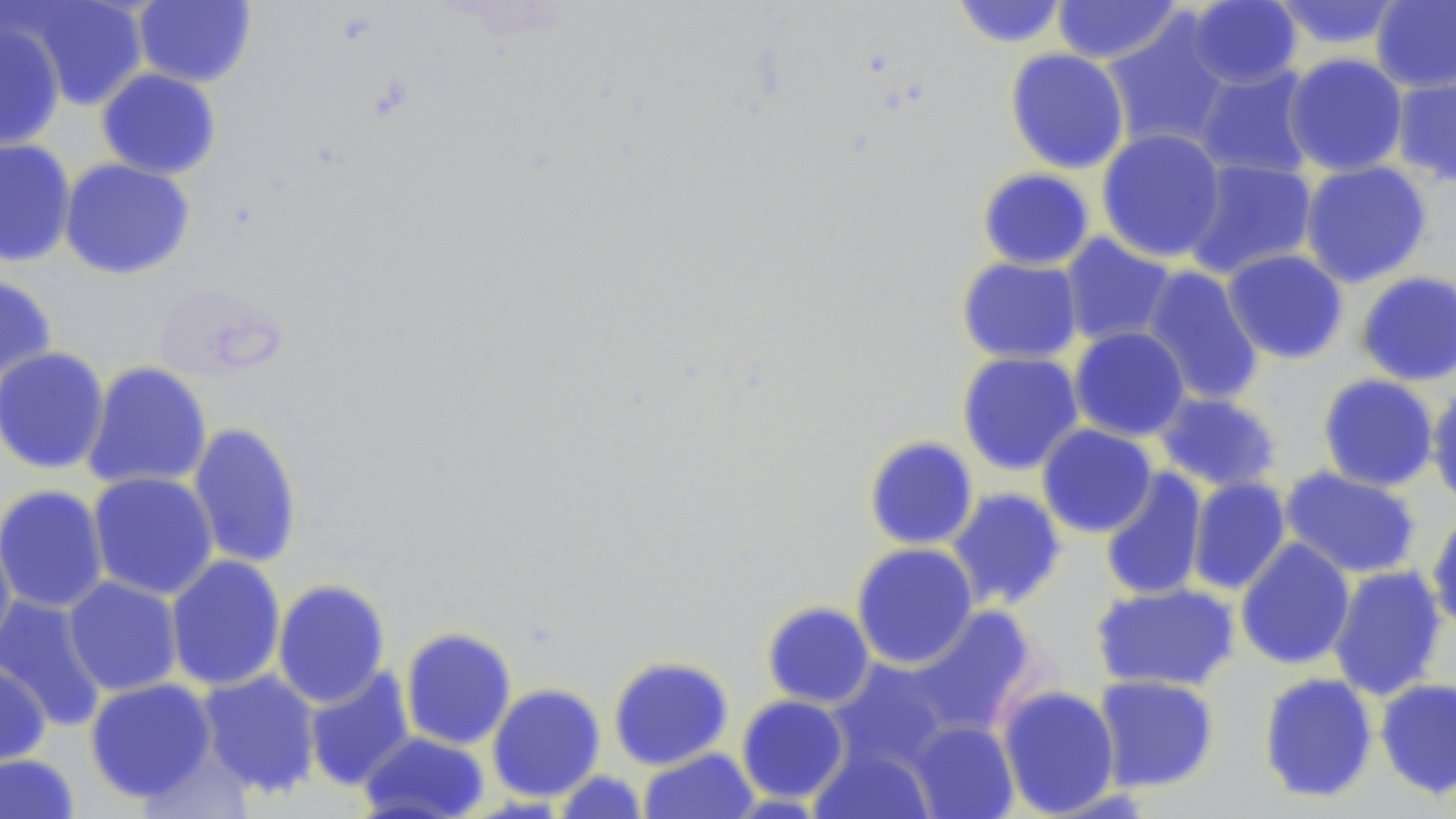 Approximate bounding boxes as named x1/y1/x2/y2 corners in pixels. Uninfected red blood cell locations: (x1=950, y1=0, x2=1071, y2=48), (x1=1051, y1=0, x2=1184, y2=65), (x1=1370, y1=0, x2=1456, y2=94), (x1=10, y1=1, x2=149, y2=110), (x1=132, y1=1, x2=257, y2=88), (x1=1185, y1=1, x2=1303, y2=90), (x1=1269, y1=1, x2=1407, y2=50), (x1=1101, y1=14, x2=1235, y2=151), (x1=0, y1=20, x2=66, y2=152), (x1=1004, y1=48, x2=1130, y2=174), (x1=1282, y1=53, x2=1409, y2=177), (x1=1191, y1=65, x2=1318, y2=180), (x1=96, y1=68, x2=222, y2=180), (x1=1391, y1=69, x2=1456, y2=188), (x1=1096, y1=128, x2=1227, y2=263), (x1=0, y1=138, x2=76, y2=268), (x1=58, y1=158, x2=196, y2=280), (x1=1182, y1=159, x2=1318, y2=280), (x1=1298, y1=161, x2=1433, y2=288), (x1=977, y1=167, x2=1095, y2=271), (x1=1059, y1=233, x2=1178, y2=348), (x1=1222, y1=249, x2=1349, y2=364), (x1=956, y1=256, x2=1083, y2=364), (x1=1140, y1=266, x2=1264, y2=407), (x1=1355, y1=271, x2=1456, y2=386), (x1=0, y1=273, x2=57, y2=386), (x1=1068, y1=326, x2=1190, y2=442), (x1=0, y1=346, x2=110, y2=476), (x1=956, y1=351, x2=1084, y2=475), (x1=82, y1=361, x2=212, y2=491), (x1=1317, y1=373, x2=1440, y2=492), (x1=1426, y1=385, x2=1456, y2=511), (x1=1151, y1=391, x2=1283, y2=493), (x1=186, y1=421, x2=304, y2=570), (x1=1036, y1=424, x2=1157, y2=538), (x1=863, y1=435, x2=979, y2=550), (x1=1279, y1=466, x2=1423, y2=580), (x1=1098, y1=467, x2=1209, y2=603), (x1=87, y1=471, x2=219, y2=601), (x1=1186, y1=476, x2=1292, y2=596), (x1=1, y1=485, x2=110, y2=614), (x1=944, y1=487, x2=1067, y2=612), (x1=1425, y1=507, x2=1456, y2=635), (x1=0, y1=523, x2=17, y2=655), (x1=1234, y1=537, x2=1356, y2=671), (x1=850, y1=542, x2=978, y2=669), (x1=165, y1=554, x2=286, y2=692), (x1=1327, y1=565, x2=1448, y2=701), (x1=63, y1=576, x2=183, y2=696), (x1=272, y1=578, x2=391, y2=708), (x1=1090, y1=582, x2=1240, y2=693), (x1=0, y1=596, x2=108, y2=731), (x1=761, y1=601, x2=875, y2=709), (x1=903, y1=605, x2=1043, y2=740), (x1=399, y1=627, x2=517, y2=750), (x1=608, y1=655, x2=733, y2=770), (x1=827, y1=657, x2=955, y2=773), (x1=0, y1=658, x2=51, y2=768), (x1=302, y1=665, x2=416, y2=792), (x1=195, y1=670, x2=322, y2=799), (x1=1257, y1=672, x2=1379, y2=804), (x1=1093, y1=674, x2=1220, y2=793), (x1=83, y1=677, x2=217, y2=804), (x1=1375, y1=677, x2=1456, y2=799), (x1=486, y1=683, x2=605, y2=802), (x1=996, y1=685, x2=1121, y2=817), (x1=736, y1=695, x2=850, y2=803), (x1=907, y1=719, x2=1020, y2=819), (x1=358, y1=731, x2=490, y2=819), (x1=810, y1=745, x2=935, y2=818), (x1=638, y1=747, x2=759, y2=819), (x1=0, y1=753, x2=81, y2=818), (x1=552, y1=769, x2=648, y2=819). Slide-level diagnosis: no evidence of blood parasites. Optical microscopy. Image is 1456×819 pixels. Single field of view. May-Grünwald-Giemsa-stained preparation. 1000x magnification. Thin blood film.